Give the extent of all Plasmodium falciparum-infected red blood cells.
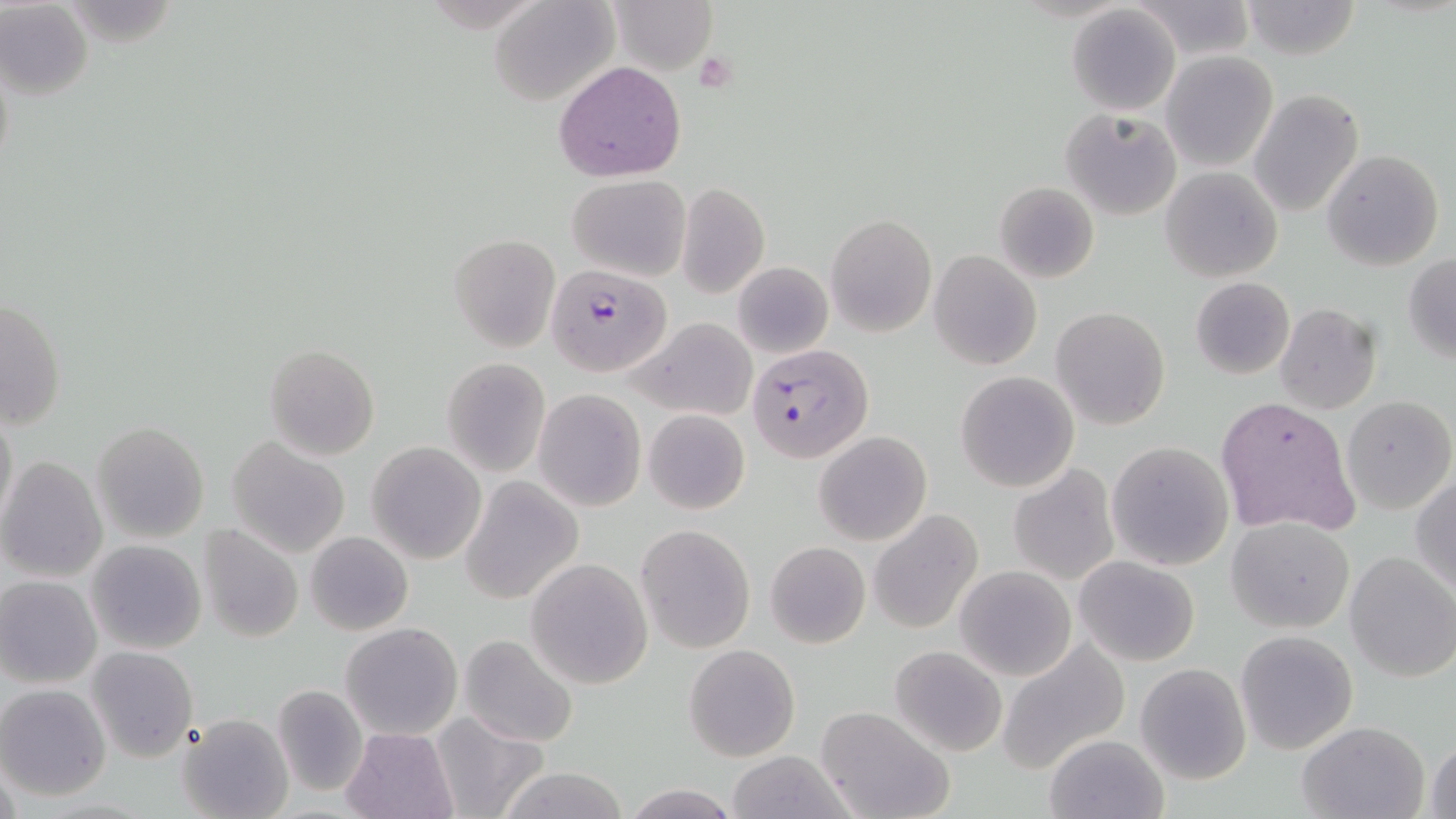

Approximate bounding boxes as [x1, y1, x2, y2] in pixels.
Plasmodium falciparum-infected red blood cells: [539, 261, 681, 382], [748, 344, 874, 463].

Platelet locations: [697, 49, 742, 92]. Uninfected red blood cell locations: [488, 0, 618, 107], [611, 0, 716, 73], [1128, 1, 1255, 61], [1240, 1, 1362, 60], [1, 2, 93, 101], [1065, 5, 1180, 115], [1160, 51, 1279, 172], [554, 61, 686, 181], [1248, 88, 1364, 218], [1060, 109, 1181, 219], [1321, 149, 1445, 271], [1160, 167, 1282, 282], [567, 173, 691, 280], [994, 181, 1099, 283], [676, 182, 769, 299], [827, 214, 936, 336], [448, 233, 560, 352], [929, 249, 1041, 370], [1403, 255, 1456, 362], [732, 261, 833, 360], [1190, 277, 1295, 379], [0, 298, 65, 432], [1275, 303, 1382, 415], [1051, 307, 1171, 430], [629, 318, 757, 420], [264, 344, 380, 461], [442, 358, 550, 476], [955, 371, 1078, 493], [535, 389, 645, 511], [1343, 395, 1454, 514], [1214, 396, 1360, 537], [1, 404, 18, 529], [643, 409, 749, 514], [91, 421, 211, 544], [814, 430, 931, 546], [226, 438, 351, 558], [1106, 441, 1234, 571], [367, 442, 487, 566], [0, 456, 107, 583], [1008, 464, 1120, 586], [1411, 474, 1456, 593], [461, 478, 583, 605], [870, 511, 984, 634], [1228, 517, 1354, 634], [197, 523, 304, 643], [636, 524, 756, 652], [305, 530, 413, 636], [85, 539, 208, 655], [766, 541, 870, 649], [1343, 550, 1456, 682], [1072, 556, 1201, 667], [525, 559, 654, 689], [955, 565, 1076, 681], [0, 576, 102, 688], [340, 622, 462, 739], [1235, 630, 1359, 755], [457, 634, 580, 747], [996, 639, 1130, 774], [685, 644, 800, 761], [85, 646, 199, 763], [890, 646, 1008, 757], [1135, 662, 1251, 785], [0, 683, 111, 801], [272, 686, 368, 797], [815, 706, 955, 819], [432, 710, 549, 819], [177, 713, 292, 819], [1296, 720, 1430, 819], [342, 729, 457, 819], [1044, 734, 1168, 818], [1425, 735, 1456, 819], [723, 750, 856, 819], [1, 757, 22, 819], [497, 766, 629, 819], [623, 783, 737, 818]. Slide-level diagnosis: Plasmodium falciparum. Thin blood film. Image is 1456×819 pixels. Light microscopy. One field of a larger specimen. 1000x magnification. May-Grünwald-Giemsa stain.